Describe the morphology of the red blood cells.
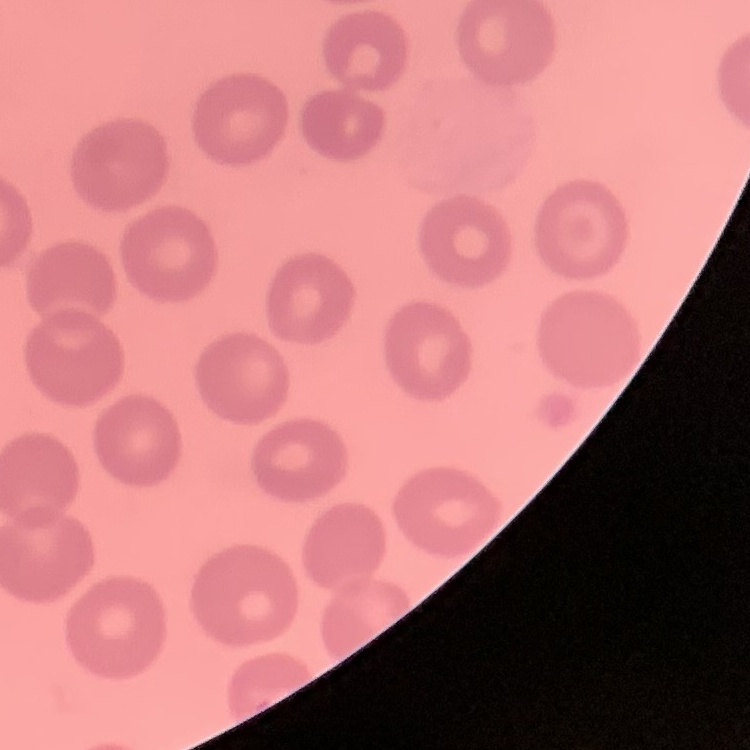

No rouleaux formation.

Field's or Giemsa stain. One tile cut from a larger photomicrograph. Thin peripheral smear.